Classify this cell by malaria status.
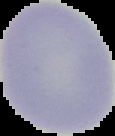

Uninfected.

Segmented cell region on a black background. Image is 115×136 pixels. From a thin blood smear.